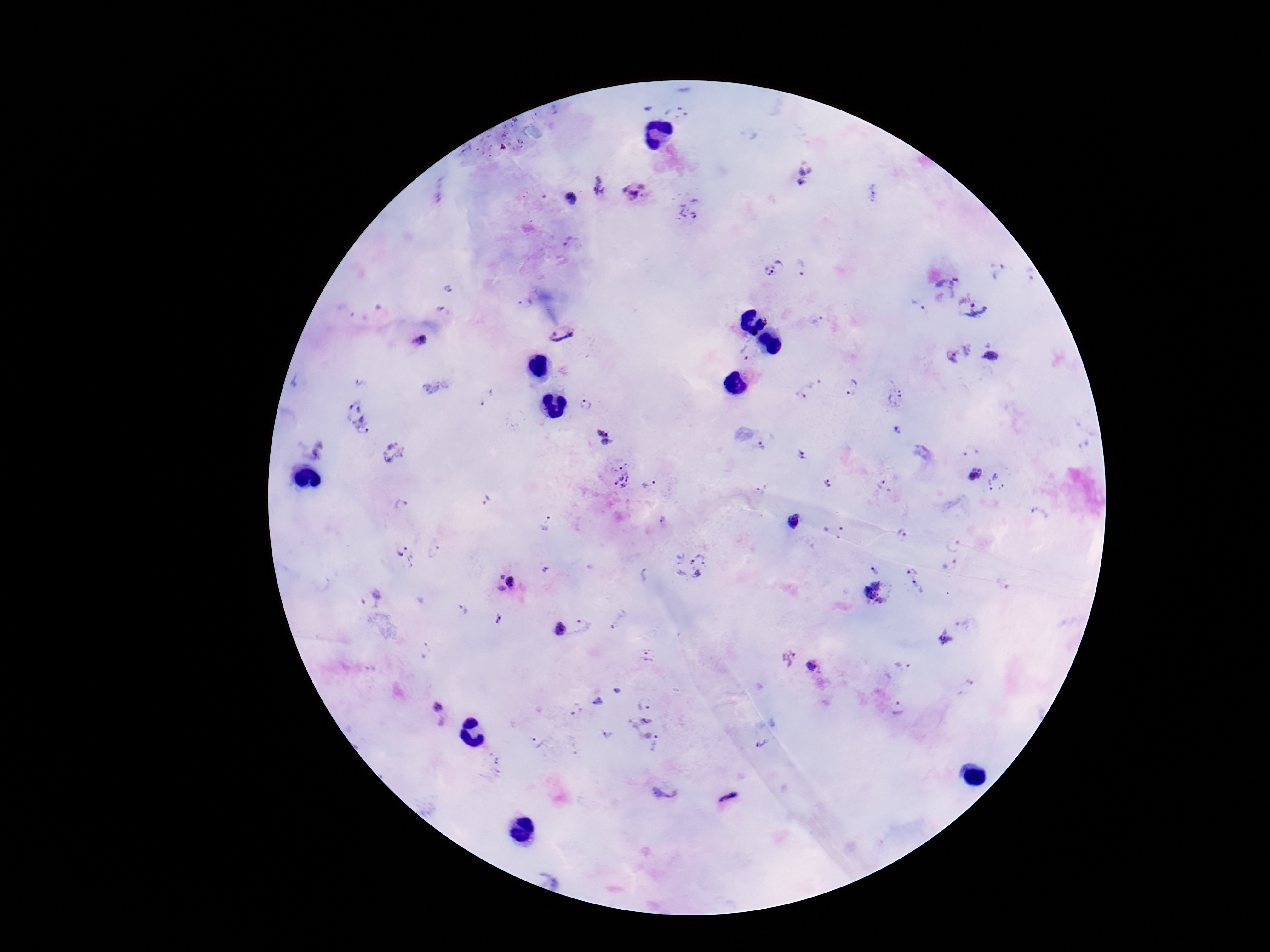
{
  "capture": "smartphone camera through the microscope eyepiece",
  "field_of_view": "single",
  "preparation": "thick blood smear",
  "stain": "Giemsa",
  "plasmodium_parasite_locations": "approximate centers as (x, y) in pixels: (806, 178), (599, 185), (871, 192), (636, 194), (571, 198), (688, 209), (573, 245), (802, 265), (775, 267), (948, 283), (450, 290), (524, 303), (918, 305), (976, 309), (440, 311), (819, 321), (561, 333), (421, 339), (746, 352), (959, 353), (992, 356), (361, 384), (814, 384), (851, 386), (487, 396), (894, 397), (798, 398), (587, 406), (361, 418), (604, 428), (896, 429), (607, 445), (760, 448), (392, 450), (801, 456), (976, 474), (617, 475), (995, 482), (647, 485), (829, 485), (885, 486), (762, 490), (486, 500), (401, 506), (1038, 516), (664, 521), (795, 523), (549, 524), (834, 531), (904, 535), (953, 545), (436, 552), (404, 556), (688, 565), (878, 568), (914, 568), (644, 575), (505, 583), (918, 586), (878, 591), (371, 597), (458, 612), (621, 617), (498, 620), (967, 620), (583, 626), (561, 630), (945, 637), (426, 652), (645, 656), (787, 657), (902, 667), (813, 668), (618, 691), (598, 700), (644, 705), (898, 709), (577, 712), (438, 714), (651, 731), (607, 734), (761, 739), (536, 742), (667, 788), (730, 800)",
  "magnification": "100x",
  "image_size": "1270×952 pixels",
  "patient_malaria_status": "infected"
}